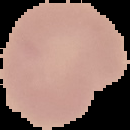

Summary:
  - Malaria status: uninfected
  - Preparation: thin blood smear
  - Image size: 130×130 pixels
  - Image type: segmented cell region with the area outside set to black